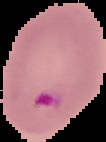
Result: Plasmodium parasites detected. From a thin blood smear. Image is 106×142 pixels. The area outside the segmented cell region is set to black.